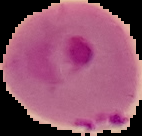
Summary:
  - Image type: segmented cell region with the area outside set to black
  - Result: malaria parasites detected
  - Preparation: thin blood film
  - Image size: 142×136 pixels